Classify this cell by malaria status.
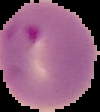
Parasitized.

From a thin blood smear. Image is 100×112 pixels. The area outside the segmented cell region is set to black.